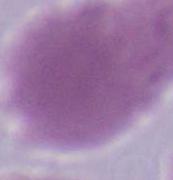
identification: red blood cell
magnification: 1000x
modality: photomicrograph